Give the extent of all Plasmodium falciparum-infected red blood cells.
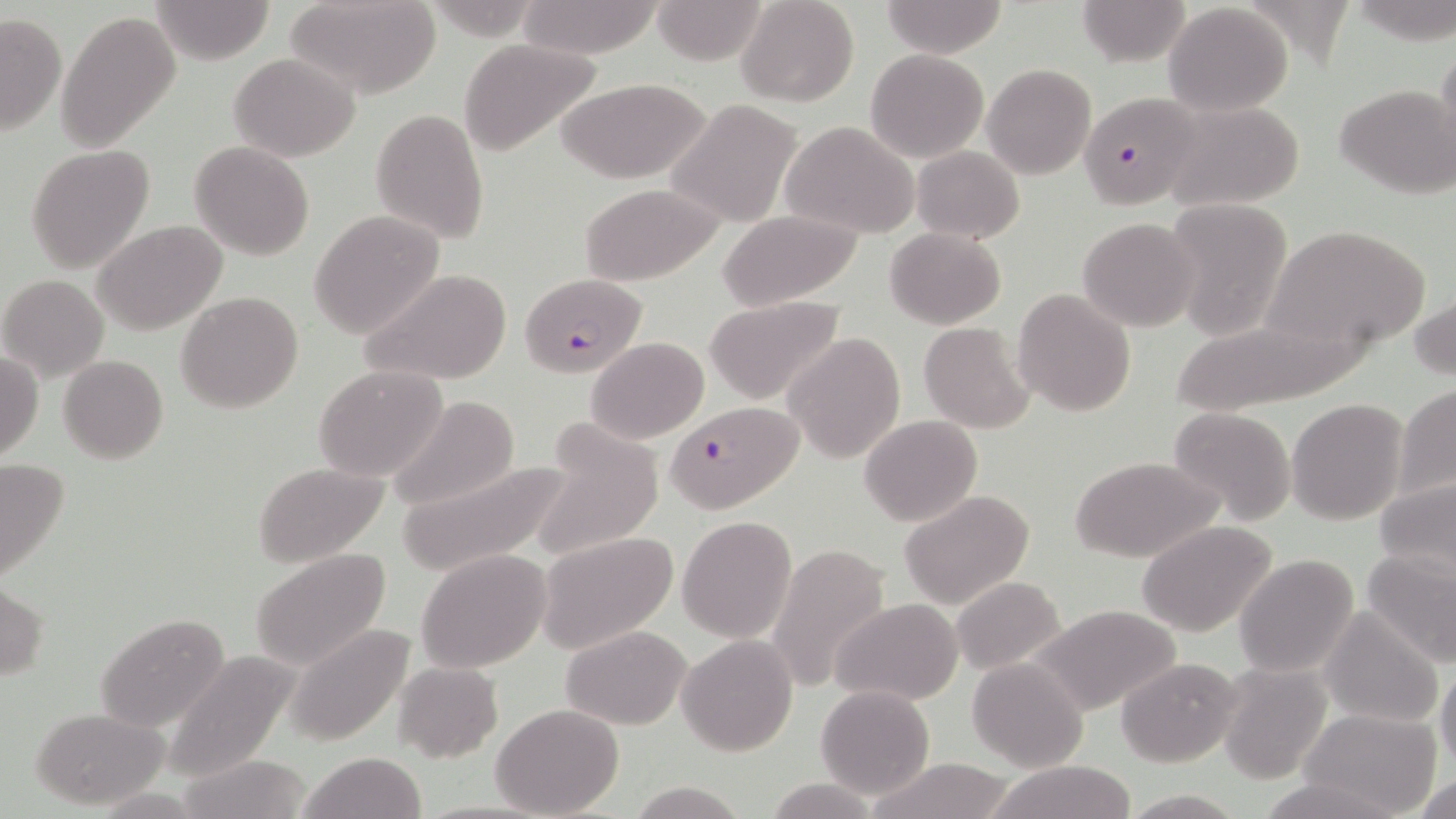

Approximate bounding boxes as (x1, y1, x2, y2) in pixels.
Plasmodium falciparum-infected red blood cells: (1077, 92, 1207, 210), (522, 272, 646, 377), (665, 399, 801, 512).

Uninfected red blood cell locations: (150, 0, 276, 65), (284, 0, 444, 99), (518, 0, 664, 59), (652, 0, 769, 65), (735, 0, 859, 107), (1075, 0, 1193, 67), (880, 1, 1007, 56), (1163, 3, 1293, 115), (56, 9, 180, 152), (0, 11, 65, 137), (459, 38, 602, 156), (1433, 39, 1456, 173), (866, 49, 987, 162), (229, 52, 361, 161), (982, 64, 1096, 179), (559, 76, 711, 184), (1334, 83, 1455, 198), (664, 99, 805, 228), (1161, 100, 1307, 212), (370, 108, 489, 245), (780, 121, 919, 239), (189, 141, 315, 260), (27, 145, 154, 270), (912, 146, 1025, 242), (579, 182, 725, 285), (1161, 199, 1293, 342), (716, 209, 866, 310), (309, 210, 444, 339), (1077, 217, 1201, 332), (94, 220, 226, 335), (1265, 224, 1431, 352), (884, 227, 1008, 329), (359, 267, 512, 387), (1, 274, 110, 383), (1012, 288, 1136, 417), (175, 291, 304, 414), (704, 295, 846, 406), (1412, 295, 1455, 383), (918, 322, 1035, 434), (783, 332, 906, 464), (586, 337, 710, 443), (0, 349, 43, 461), (59, 355, 168, 464), (314, 364, 447, 482), (1395, 384, 1456, 503), (385, 395, 521, 514), (1286, 398, 1409, 525), (1169, 407, 1296, 526), (859, 414, 982, 527), (531, 428, 664, 561), (1072, 456, 1222, 563), (0, 459, 71, 585), (394, 460, 573, 577), (250, 461, 391, 568), (1373, 477, 1456, 584), (900, 491, 1034, 609), (677, 516, 797, 642), (1137, 519, 1281, 638), (537, 531, 678, 654), (768, 544, 892, 692), (248, 548, 393, 674), (1361, 548, 1456, 668), (415, 549, 552, 674), (1235, 553, 1359, 677), (951, 576, 1067, 675), (0, 582, 48, 682), (832, 598, 962, 705), (1031, 603, 1183, 717), (1320, 607, 1443, 729), (96, 612, 230, 733), (285, 624, 414, 745), (562, 626, 692, 729), (677, 635, 797, 756), (163, 648, 299, 781), (1116, 656, 1242, 767), (967, 658, 1088, 771), (393, 661, 502, 762), (1217, 661, 1333, 785), (1436, 663, 1456, 773), (815, 685, 937, 798), (492, 703, 625, 818), (31, 707, 168, 808), (1302, 707, 1441, 816), (299, 752, 425, 819), (865, 758, 1017, 819), (986, 762, 1137, 819), (1410, 773, 1456, 819), (1256, 775, 1400, 819), (763, 777, 883, 818), (628, 779, 748, 818), (1121, 789, 1246, 819). Slide-level diagnosis: Plasmodium falciparum. Light microscopy. May-Grünwald-Giemsa-stained preparation. Captured at 1000x magnification. Single field of view. Image is 1456×819 pixels. Thin blood smear.